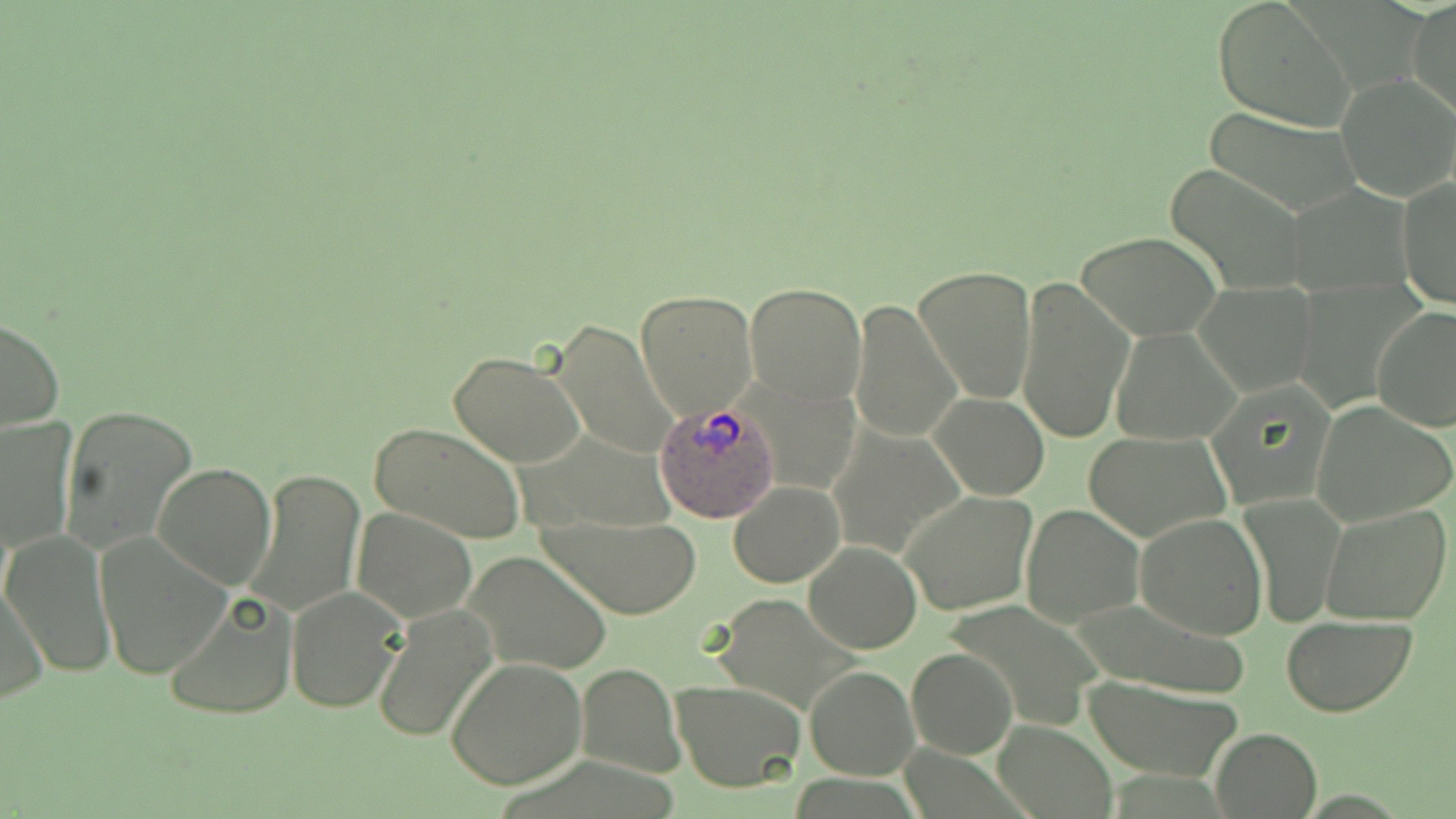 Approximate bounding boxes as (x1,y1)-(x2,y2) corner pairs in pixels. Plasmodium ovale-infected red blood cell locations: (652,402)-(779,522). Uninfected red blood cell locations: (1408,0)-(1455,119), (1211,1)-(1356,131), (1338,75)-(1455,200), (1200,107)-(1366,216), (1167,166)-(1306,294), (1397,177)-(1455,310), (1079,232)-(1222,340), (912,265)-(1038,405), (1016,275)-(1132,441), (744,282)-(866,406), (1195,282)-(1318,396), (636,287)-(756,419), (850,298)-(961,443), (1372,307)-(1456,430), (0,318)-(65,432), (548,319)-(678,460), (1110,326)-(1241,445), (447,350)-(588,468), (930,393)-(1049,500), (1312,400)-(1454,526), (60,406)-(198,555), (1,417)-(76,556), (367,421)-(526,548), (828,423)-(967,561), (1083,430)-(1230,541), (152,462)-(276,591), (247,469)-(366,617), (729,481)-(844,587), (901,491)-(1036,616), (1242,492)-(1344,629), (1321,503)-(1451,625), (1021,504)-(1143,628), (352,507)-(477,623), (544,510)-(699,620), (1136,513)-(1268,640), (95,527)-(233,677), (4,531)-(116,676), (805,543)-(921,654), (464,551)-(612,674), (1,578)-(50,706), (286,584)-(407,713), (165,590)-(299,722), (371,606)-(498,742), (1281,617)-(1414,716), (905,647)-(1017,759), (447,658)-(588,790), (577,662)-(683,778), (805,666)-(917,780), (1080,673)-(1244,783), (672,679)-(806,792), (993,719)-(1115,817), (1209,727)-(1322,819). Slide-level diagnosis: Plasmodium ovale. Thin blood smear. 1000x magnification. Light microscopy. Image is 1456×819 pixels. One field of a larger specimen. May-Grünwald-Giemsa stain.